State which parasite is depicted.
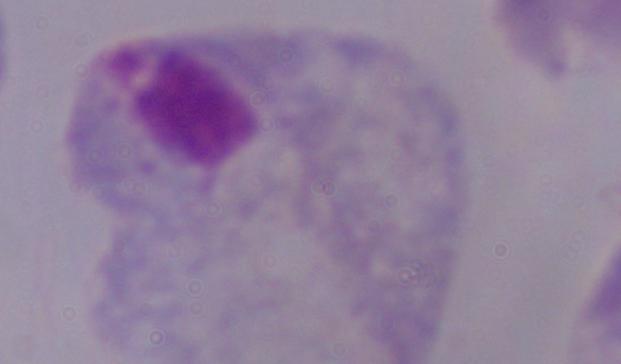
This is a trichomonad.

Summary:
  - Modality: photomicrograph
  - Magnification: 1000x